Assess this cell for malaria.
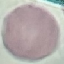

Uninfected.

Cell patch, automatically extracted from a larger field of view and resized to 64 × 64 pixels. Thin blood smear. Photographed with a smartphone camera at the microscope eyepiece. Giemsa stain.